Assess this cell for malaria.
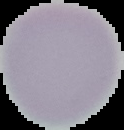

Uninfected.

The area outside the segmented cell region is set to black. Image is 124×130 pixels. From a thin blood smear.